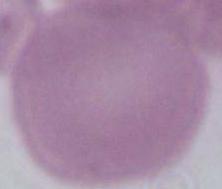

magnification = 1000x
modality = micrograph
identification = red blood cell